Outline each blood parasite and name the species.
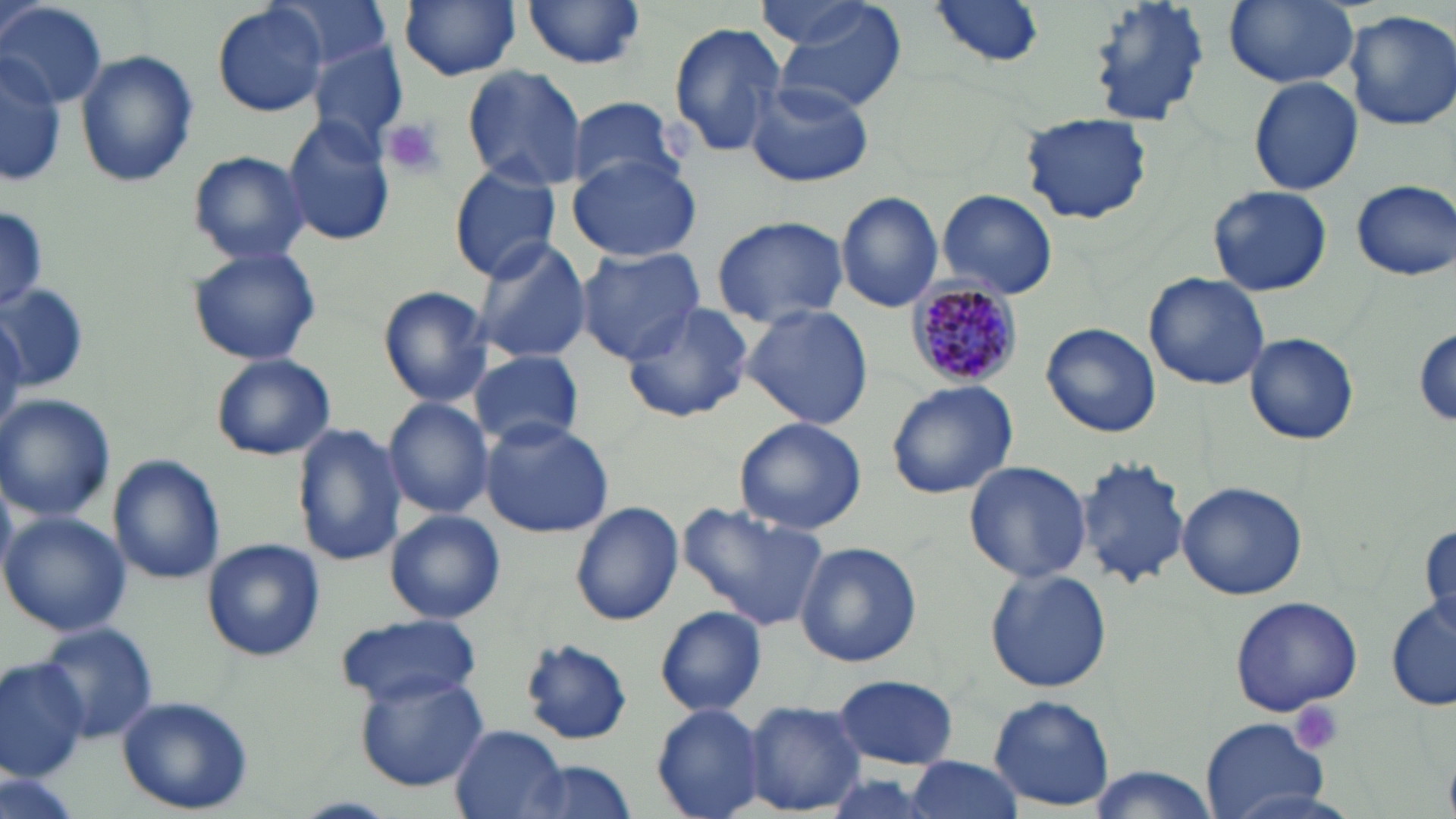
Approximate bounding boxes as named x1/y1/x2/y2 corners in pixels.
Plasmodium malariae-infected red blood cells: (x1=907, y1=282, x2=1023, y2=385).
No Plasmodium falciparum, Plasmodium ovale, Plasmodium vivax, Babesia divergens, or Trypanosoma brucei observed.

Platelet locations: (x1=382, y1=117, x2=445, y2=178), (x1=1290, y1=701, x2=1345, y2=756). Uninfected red blood cell locations: (x1=271, y1=0, x2=393, y2=75), (x1=399, y1=0, x2=521, y2=81), (x1=926, y1=0, x2=1049, y2=69), (x1=1087, y1=0, x2=1212, y2=128), (x1=1223, y1=0, x2=1362, y2=89), (x1=770, y1=1, x2=910, y2=113), (x1=521, y1=2, x2=649, y2=70), (x1=0, y1=3, x2=107, y2=108), (x1=211, y1=3, x2=330, y2=118), (x1=753, y1=3, x2=894, y2=50), (x1=1344, y1=9, x2=1456, y2=132), (x1=664, y1=19, x2=787, y2=161), (x1=309, y1=42, x2=409, y2=150), (x1=76, y1=50, x2=197, y2=188), (x1=0, y1=55, x2=66, y2=186), (x1=460, y1=65, x2=586, y2=188), (x1=1248, y1=75, x2=1362, y2=196), (x1=743, y1=78, x2=873, y2=189), (x1=566, y1=95, x2=684, y2=197), (x1=1022, y1=111, x2=1152, y2=226), (x1=283, y1=117, x2=397, y2=247), (x1=187, y1=150, x2=310, y2=264), (x1=568, y1=154, x2=700, y2=263), (x1=449, y1=164, x2=561, y2=282), (x1=1351, y1=179, x2=1456, y2=281), (x1=1208, y1=184, x2=1333, y2=297), (x1=935, y1=188, x2=1059, y2=300), (x1=836, y1=190, x2=944, y2=312), (x1=0, y1=201, x2=46, y2=312), (x1=1174, y1=207, x2=1301, y2=349), (x1=710, y1=215, x2=849, y2=327), (x1=470, y1=237, x2=591, y2=364), (x1=187, y1=246, x2=322, y2=366), (x1=574, y1=247, x2=707, y2=363), (x1=1142, y1=271, x2=1272, y2=391), (x1=0, y1=283, x2=92, y2=391), (x1=377, y1=286, x2=494, y2=406), (x1=620, y1=301, x2=756, y2=423), (x1=741, y1=304, x2=875, y2=428), (x1=0, y1=307, x2=26, y2=444), (x1=1040, y1=321, x2=1163, y2=439), (x1=1412, y1=325, x2=1456, y2=431), (x1=1245, y1=333, x2=1359, y2=445), (x1=470, y1=349, x2=584, y2=451), (x1=210, y1=355, x2=336, y2=461), (x1=884, y1=380, x2=1019, y2=500), (x1=0, y1=394, x2=116, y2=523), (x1=382, y1=395, x2=494, y2=520), (x1=733, y1=416, x2=868, y2=534), (x1=477, y1=419, x2=615, y2=537), (x1=293, y1=424, x2=406, y2=567), (x1=1073, y1=454, x2=1192, y2=588), (x1=109, y1=455, x2=226, y2=584), (x1=961, y1=460, x2=1093, y2=585), (x1=1176, y1=481, x2=1309, y2=601), (x1=678, y1=500, x2=829, y2=632), (x1=571, y1=502, x2=683, y2=625), (x1=0, y1=509, x2=131, y2=639), (x1=383, y1=509, x2=506, y2=624), (x1=1419, y1=524, x2=1456, y2=635), (x1=201, y1=538, x2=325, y2=661), (x1=795, y1=541, x2=922, y2=667), (x1=985, y1=567, x2=1112, y2=693), (x1=1229, y1=595, x2=1363, y2=716), (x1=1386, y1=600, x2=1456, y2=711), (x1=655, y1=607, x2=767, y2=716), (x1=332, y1=612, x2=481, y2=707), (x1=36, y1=620, x2=157, y2=743), (x1=521, y1=638, x2=634, y2=745), (x1=0, y1=658, x2=89, y2=784), (x1=834, y1=673, x2=959, y2=768), (x1=356, y1=674, x2=489, y2=792), (x1=989, y1=694, x2=1114, y2=812), (x1=116, y1=695, x2=254, y2=814), (x1=742, y1=700, x2=865, y2=815), (x1=652, y1=704, x2=768, y2=818), (x1=1200, y1=719, x2=1329, y2=817), (x1=451, y1=726, x2=573, y2=819), (x1=903, y1=756, x2=1026, y2=819), (x1=509, y1=761, x2=640, y2=819), (x1=1088, y1=765, x2=1212, y2=818), (x1=2, y1=767, x2=83, y2=819). Slide-level diagnosis: Plasmodium malariae. May-Grünwald-Giemsa-stained preparation. Thin blood smear. Image is 1456×819 pixels. 1000x magnification. Light microscopy. Single field of view.